Outline each blood parasite and name the species.
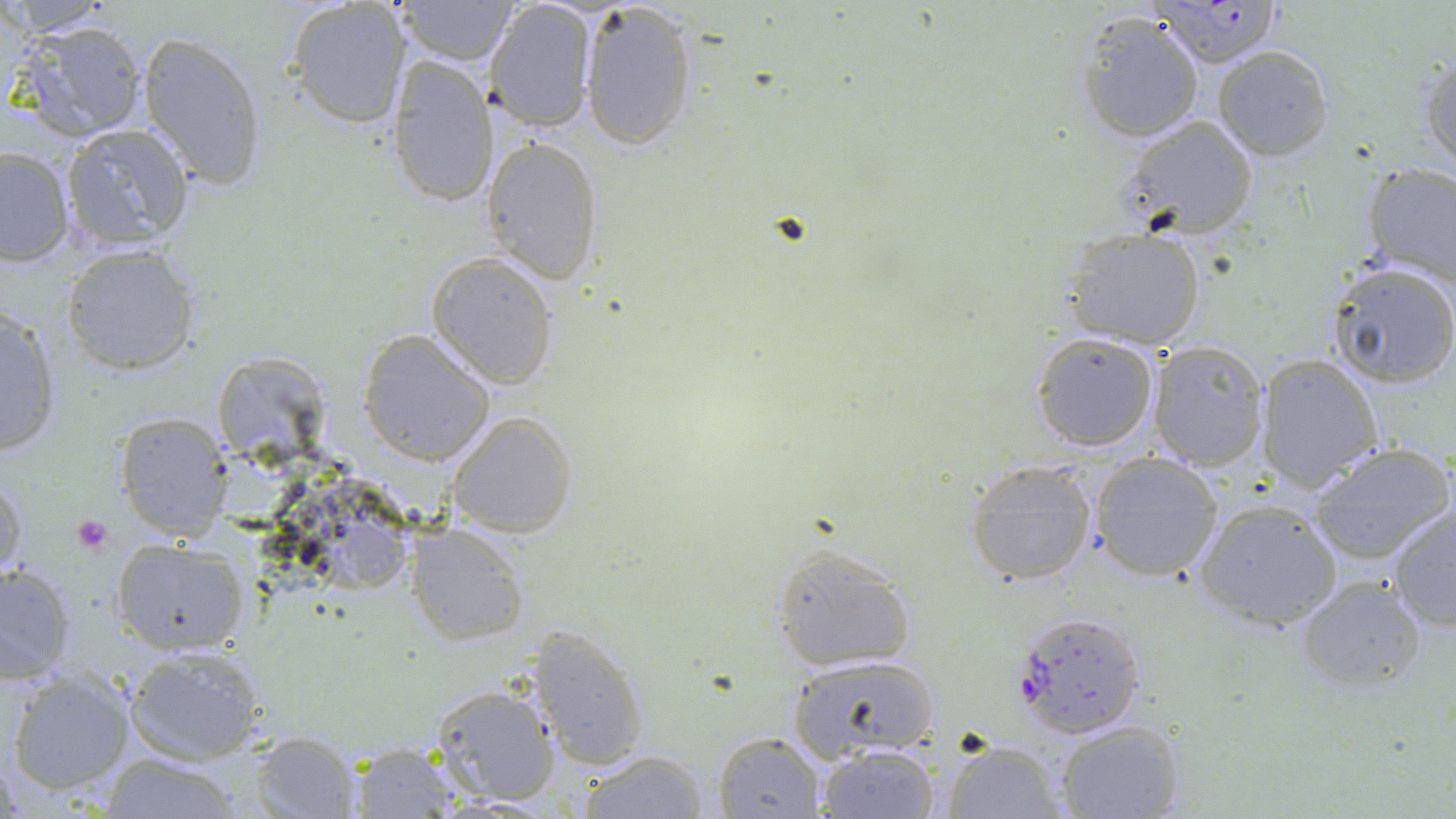

Approximate bounding boxes as (x1, y1, x2, y2) in pixels.
Plasmodium falciparum-infected red blood cells: (1149, 0, 1285, 66), (1013, 610, 1147, 738).
No Plasmodium ovale, Plasmodium malariae, Plasmodium vivax, Babesia divergens, or Trypanosoma brucei observed.

{
  "slide_level_diagnosis": "Plasmodium falciparum",
  "stain": "May-Grünwald-Giemsa",
  "magnification": "1000x",
  "modality": "light microscopy",
  "field_of_view": "one of a larger specimen",
  "platelet_locations": "approximate bounding boxes as (x1, y1, x2, y2) in pixels: (71, 515, 112, 555)",
  "uninfected_red_blood_cell_locations": "approximate bounding boxes as (x1, y1, x2, y2) in pixels: (396, 0, 510, 64), (579, 0, 700, 151), (2, 1, 116, 35), (282, 1, 409, 129), (487, 3, 598, 132), (1076, 11, 1205, 143), (9, 19, 151, 143), (137, 30, 268, 192), (1212, 45, 1334, 161), (387, 54, 497, 210), (1421, 55, 1455, 172), (1115, 116, 1260, 240), (60, 125, 196, 251), (482, 136, 606, 286), (0, 145, 76, 268), (1359, 163, 1456, 290), (1061, 226, 1208, 350), (62, 244, 199, 377), (427, 253, 559, 389), (1326, 262, 1456, 387), (0, 307, 63, 456), (1030, 331, 1160, 453), (358, 332, 494, 466), (1148, 340, 1269, 467), (1255, 353, 1384, 493), (221, 358, 324, 469), (447, 411, 577, 538), (113, 412, 233, 539), (1307, 442, 1455, 566), (1087, 455, 1224, 582), (964, 461, 1099, 585), (1, 469, 27, 585), (301, 480, 406, 594), (1192, 498, 1342, 631), (1386, 499, 1455, 634), (406, 524, 529, 646), (112, 539, 249, 655), (768, 542, 920, 674), (0, 560, 79, 684), (1294, 575, 1428, 694), (527, 625, 650, 770), (122, 643, 268, 763), (786, 655, 941, 763), (6, 667, 135, 799), (428, 683, 561, 808), (1052, 721, 1185, 819), (249, 730, 360, 817), (713, 730, 828, 818), (939, 738, 1066, 818), (816, 743, 942, 819), (343, 745, 465, 816), (573, 747, 711, 819), (98, 756, 249, 817)",
  "image_size": "1456×819 pixels",
  "preparation": "thin blood film"
}